State which parasite is depicted.
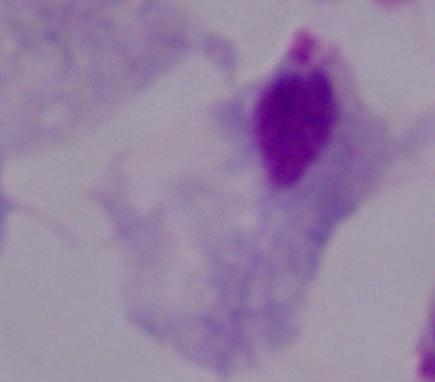

This is a trichomonad.

Summary:
  - Magnification: 1000x
  - Modality: photomicrograph